Classify this cell by malaria status.
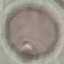

Uninfected.

Photographed with a smartphone camera at the microscope eyepiece. Giemsa-stained preparation. Thin smear of blood. Automatically extracted cell patch, resized to 64 × 64 pixels.